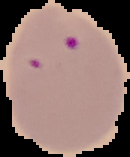
Segmented cell region on a black background. From a thin blood smear. Image is 130×157 pixels. Malaria status: parasitized.